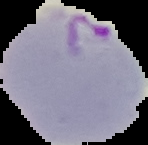 Image is 148×145 pixels. From a thin blood smear. Malaria status: parasitized. Segmented cell region on a black background.